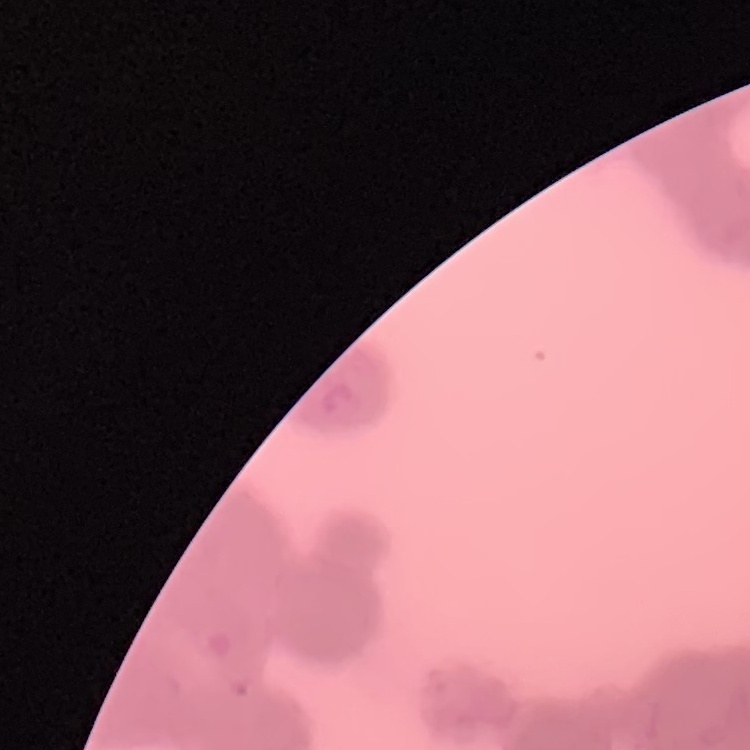
The erythrocytes exhibit rouleaux formation. One tile cut from a larger photomicrograph. Thin blood smear. Field's or Giemsa stain.